Identify the blood parasite species.
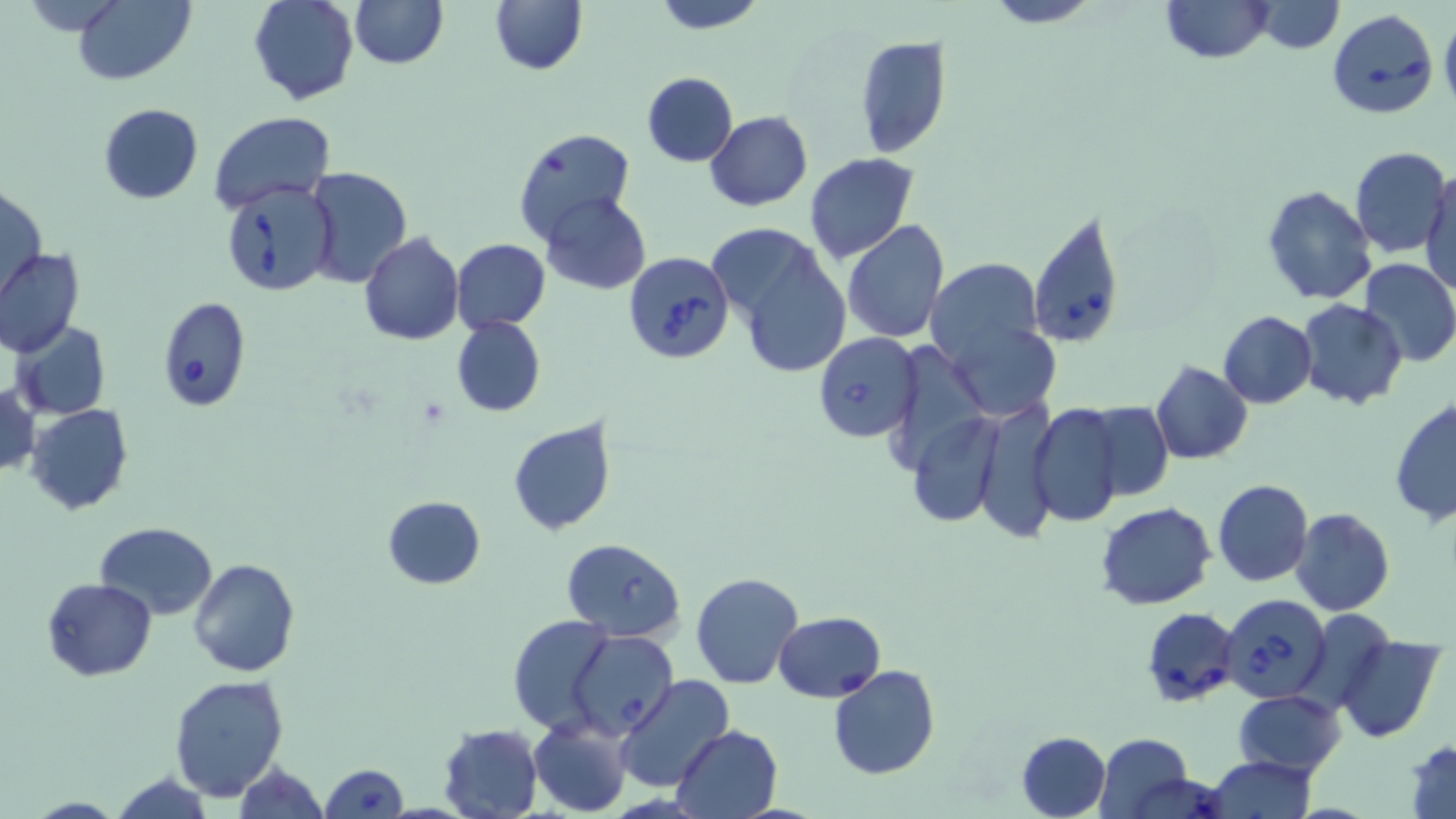
Babesia divergens.

Approximate bounding boxes as (x1,y1)-(x2,y2) corner pairs in pixels. Uninfected red blood cell locations: (71,0)-(194,85), (247,0)-(359,106), (349,0)-(447,69), (489,0)-(587,76), (652,0)-(766,32), (983,0)-(1101,27), (1159,0)-(1273,63), (1250,2)-(1346,53), (1440,15)-(1456,112), (855,33)-(950,159), (642,73)-(737,167), (98,104)-(204,203), (209,111)-(335,216), (706,111)-(813,211), (512,128)-(638,246), (1350,147)-(1451,259), (804,153)-(917,263), (302,166)-(413,288), (1422,166)-(1456,295), (2,182)-(47,301), (1262,184)-(1377,305), (541,193)-(650,294), (842,219)-(951,343), (709,221)-(852,378), (360,233)-(464,345), (451,238)-(549,332), (0,247)-(84,357), (925,256)-(1049,373), (1358,258)-(1456,368), (1297,299)-(1407,409), (1218,311)-(1317,409), (942,314)-(1062,421), (451,315)-(545,417), (12,323)-(111,421), (1151,361)-(1252,464), (0,382)-(39,479), (1389,394)-(1455,526), (1084,399)-(1174,500), (969,401)-(1057,541), (1028,402)-(1125,527), (24,404)-(134,515), (506,417)-(618,536), (1212,479)-(1313,587), (382,496)-(485,589), (1098,502)-(1216,609), (1290,508)-(1394,616), (94,521)-(219,619), (561,538)-(686,641), (187,557)-(300,678), (690,571)-(804,689), (43,578)-(157,681), (508,615)-(619,736), (1338,636)-(1446,742), (827,665)-(941,781), (168,674)-(290,802), (615,674)-(737,793), (1233,690)-(1346,776), (528,717)-(632,817), (439,724)-(543,819), (670,726)-(782,817), (1016,731)-(1111,819), (1096,732)-(1195,817), (1405,739)-(1456,819), (1206,757)-(1316,818), (230,761)-(328,818), (320,763)-(408,818), (106,770)-(220,819). Babesia divergens-infected red blood cell locations: (1326,9)-(1438,118), (222,180)-(340,298), (1027,212)-(1124,348), (624,252)-(734,364), (157,295)-(252,412), (813,331)-(920,441), (1220,592)-(1335,705), (1142,607)-(1241,710), (774,612)-(885,702), (570,631)-(676,739). May-Grünwald-Giemsa-stained preparation. Captured at 1000x magnification. One field of a larger specimen. Thin blood film. Image is 1456×819 pixels. Light microscopy.